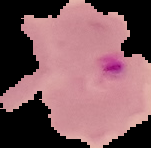

Summary:
  - Image type: segmented cell region with the area outside set to black
  - Preparation: thin blood film
  - Image size: 151×148 pixels
  - Result: Plasmodium parasites identified